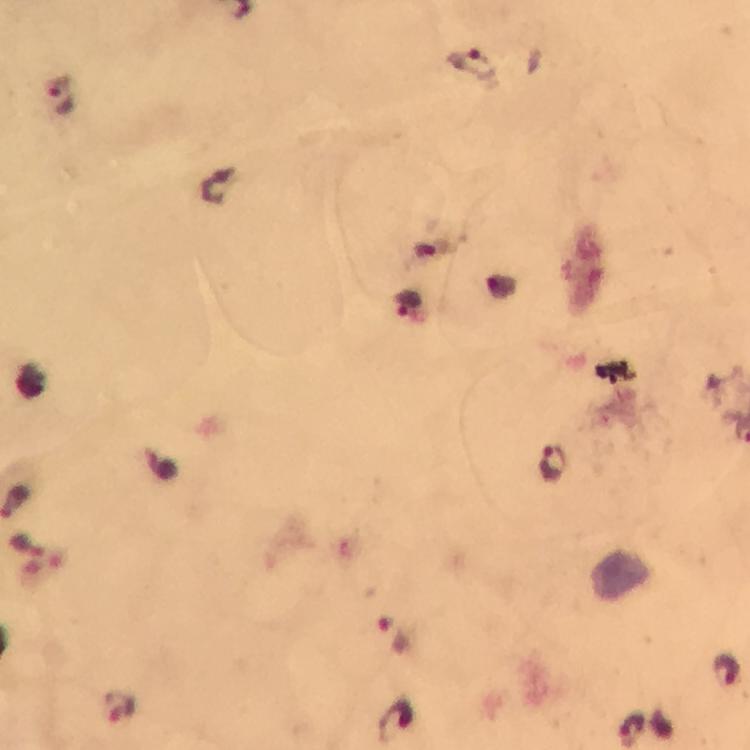

cropped from = a single field of view
capture = smartphone camera through the microscope
magnification = 100x
malaria parasite locations = approximate object centers, in pixels from the top-left corner: (x=473, y=62), (x=60, y=93), (x=408, y=304), (x=550, y=463), (x=392, y=635), (x=727, y=671), (x=120, y=705), (x=393, y=718), (x=632, y=729)
stain = Giemsa
immersion oil = used
preparation = thick blood smear
image size = 750×750 pixels
context = from a malaria diagnostic workup